State which parasite is depicted.
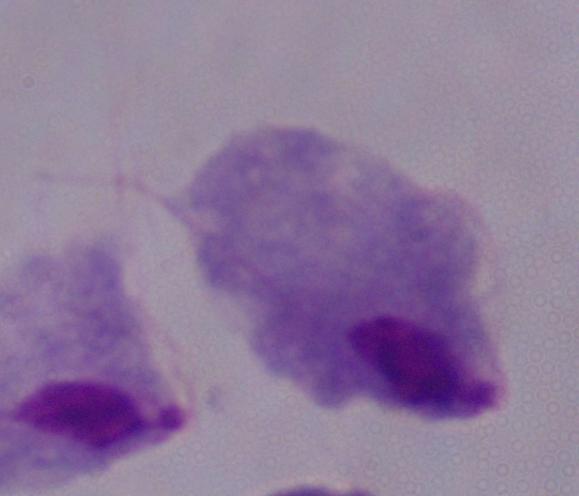
This is a trichomonad.

modality = micrograph
magnification = 1000x